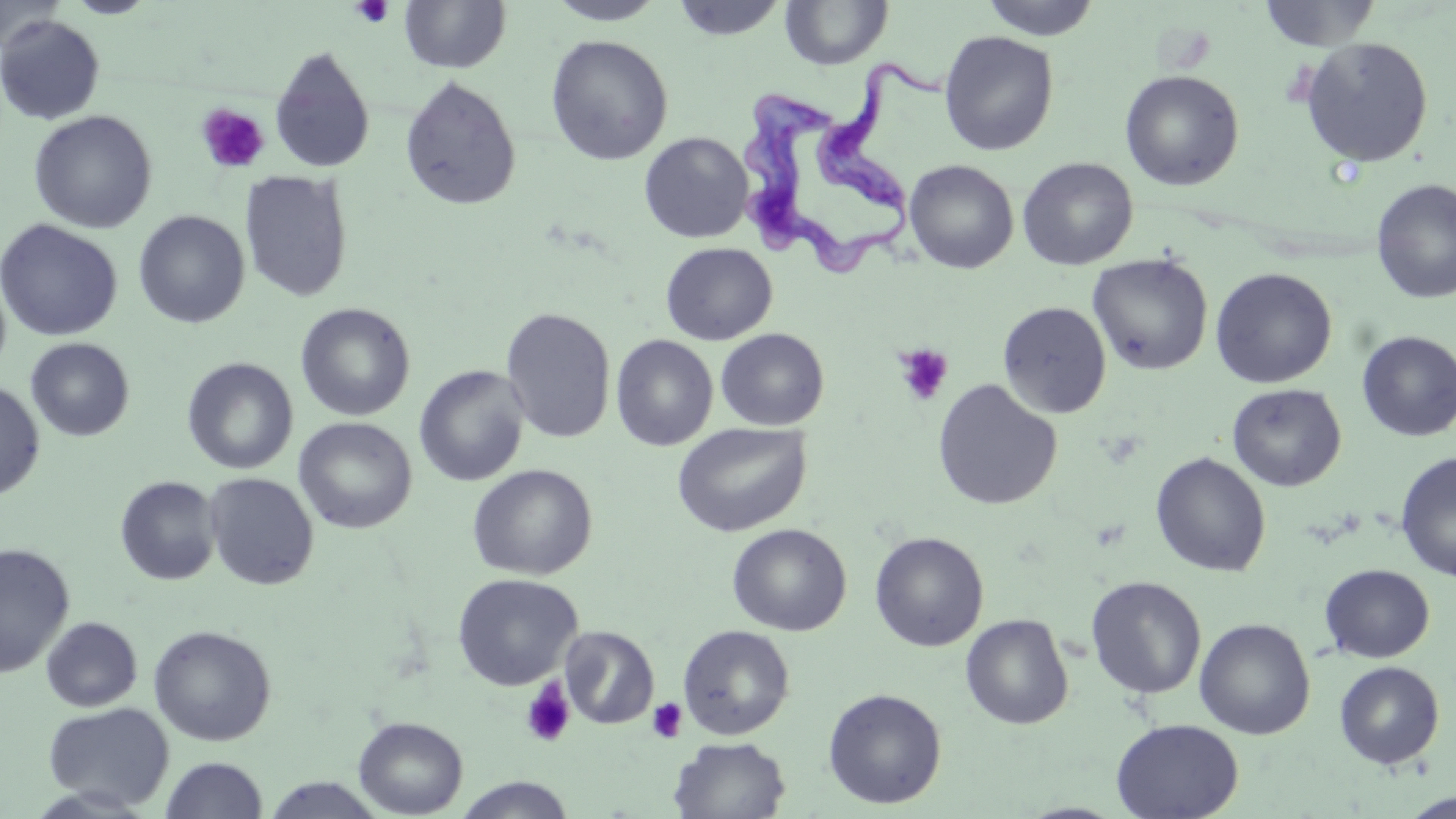
slide_level_diagnosis: Trypanosoma brucei
field_of_view: one of a larger specimen
stain: May-Grünwald-Giemsa
uninfected_red_blood_cell_locations: 'approximate bounding boxes as named x1/y1/x2/y2 corners in pixels: (x1=0, y1=0, x2=65, y2=55), (x1=399, y1=0, x2=511, y2=73), (x1=546, y1=0, x2=667, y2=25), (x1=670, y1=0, x2=788, y2=41), (x1=979, y1=0, x2=1102, y2=40), (x1=1257, y1=0, x2=1382, y2=51), (x1=779, y1=1, x2=894, y2=70), (x1=0, y1=15, x2=105, y2=125), (x1=938, y1=30, x2=1059, y2=156), (x1=546, y1=34, x2=673, y2=166), (x1=1299, y1=37, x2=1434, y2=168), (x1=269, y1=45, x2=376, y2=174), (x1=1120, y1=69, x2=1244, y2=191), (x1=399, y1=75, x2=522, y2=212), (x1=29, y1=110, x2=157, y2=233), (x1=639, y1=132, x2=753, y2=243), (x1=1017, y1=157, x2=1138, y2=270), (x1=904, y1=160, x2=1018, y2=274), (x1=240, y1=169, x2=354, y2=303), (x1=1371, y1=179, x2=1456, y2=304), (x1=133, y1=210, x2=249, y2=328), (x1=0, y1=219, x2=123, y2=341), (x1=661, y1=243, x2=777, y2=345), (x1=1087, y1=253, x2=1213, y2=375), (x1=1210, y1=267, x2=1337, y2=388), (x1=0, y1=268, x2=12, y2=380), (x1=997, y1=301, x2=1111, y2=418), (x1=296, y1=302, x2=415, y2=421), (x1=500, y1=307, x2=616, y2=444), (x1=715, y1=328, x2=829, y2=431), (x1=1356, y1=330, x2=1456, y2=442), (x1=611, y1=334, x2=718, y2=450), (x1=25, y1=337, x2=135, y2=441), (x1=182, y1=357, x2=298, y2=475), (x1=414, y1=365, x2=530, y2=487), (x1=0, y1=379, x2=45, y2=501), (x1=932, y1=379, x2=1062, y2=511), (x1=1227, y1=383, x2=1346, y2=492), (x1=294, y1=417, x2=417, y2=534), (x1=672, y1=422, x2=811, y2=537), (x1=1394, y1=451, x2=1456, y2=582), (x1=1150, y1=452, x2=1271, y2=577), (x1=467, y1=464, x2=597, y2=580), (x1=204, y1=472, x2=319, y2=590), (x1=115, y1=475, x2=221, y2=585), (x1=727, y1=523, x2=852, y2=636), (x1=869, y1=531, x2=989, y2=651), (x1=0, y1=542, x2=75, y2=678), (x1=1319, y1=564, x2=1435, y2=663), (x1=452, y1=573, x2=583, y2=691), (x1=1085, y1=576, x2=1207, y2=700), (x1=960, y1=614, x2=1073, y2=730), (x1=40, y1=616, x2=142, y2=712), (x1=1194, y1=617, x2=1316, y2=740), (x1=148, y1=624, x2=277, y2=746), (x1=677, y1=624, x2=795, y2=740), (x1=559, y1=625, x2=659, y2=730), (x1=1334, y1=660, x2=1445, y2=769), (x1=823, y1=687, x2=947, y2=808), (x1=42, y1=702, x2=174, y2=811), (x1=353, y1=716, x2=468, y2=817), (x1=1110, y1=717, x2=1244, y2=819), (x1=669, y1=736, x2=791, y2=819), (x1=161, y1=756, x2=268, y2=818), (x1=453, y1=775, x2=575, y2=818), (x1=260, y1=777, x2=387, y2=818), (x1=1399, y1=791, x2=1455, y2=818)'
magnification: 1000x
platelet_locations: 'approximate bounding boxes as named x1/y1/x2/y2 corners in pixels: (x1=350, y1=0, x2=395, y2=28), (x1=196, y1=103, x2=270, y2=174), (x1=893, y1=343, x2=954, y2=407), (x1=519, y1=680, x2=576, y2=748), (x1=647, y1=697, x2=688, y2=743)'
trypanosoma_brucei_locations: 'approximate bounding boxes as named x1/y1/x2/y2 corners in pixels: (x1=739, y1=53, x2=952, y2=287)'
modality: optical microscopy
image_size: 1456×819 pixels
preparation: thin blood film